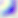
Summary:
  - Identification: Toxoplasma gondii
  - Modality: photomicrograph
  - Magnification: 400x